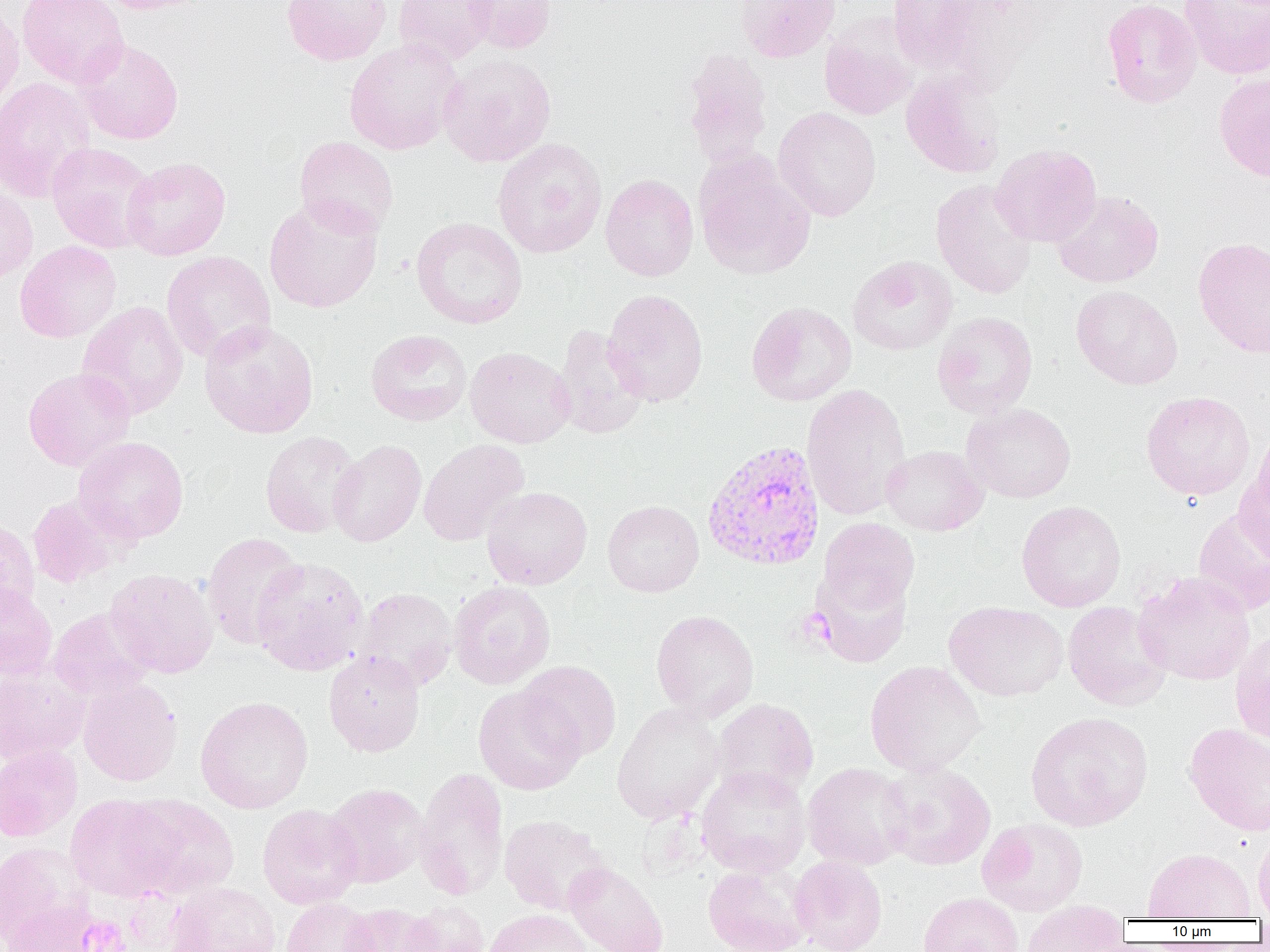

Summary:
  - Coordinate format: approximate bounding boxes as (x1,y1)-(x2,y2) corner pairs in pixels
  - Plasmodium vivax-infected red blood cell locations: (701,440)-(825,572)
  - Uninfected red blood cell locations: (17,0)-(129,88), (92,0)-(213,14), (281,0)-(391,65), (393,0)-(496,66), (463,0)-(556,54), (735,0)-(840,62), (888,0)-(977,71), (1102,0)-(1202,108), (1180,0)-(1270,79), (0,3)-(24,114), (820,24)-(917,120), (73,38)-(184,145), (343,38)-(464,155), (681,49)-(774,167), (438,53)-(557,167), (901,69)-(1006,178), (1215,73)-(1270,181), (0,77)-(97,203), (773,107)-(882,221), (294,136)-(399,237), (493,138)-(607,258), (46,142)-(157,253), (990,144)-(1102,247), (121,156)-(231,260), (695,158)-(816,280), (600,174)-(699,281), (930,180)-(1037,300), (0,182)-(38,284), (1051,190)-(1164,288), (263,196)-(384,314), (411,216)-(528,329), (1193,237)-(1270,358), (14,240)-(121,343), (161,251)-(276,363), (847,256)-(957,355), (1071,285)-(1183,389), (602,289)-(709,407), (76,301)-(188,419), (747,301)-(856,406), (932,311)-(1037,418), (199,319)-(319,439), (552,325)-(649,439), (365,329)-(472,426), (465,347)-(576,448), (23,367)-(136,471), (802,383)-(911,520), (1140,390)-(1256,501), (961,403)-(1076,503), (259,431)-(363,538), (73,436)-(189,544), (329,439)-(427,547), (418,439)-(529,546), (881,445)-(988,535), (1234,466)-(1270,566), (481,486)-(592,590), (27,495)-(124,588), (603,500)-(704,597), (1016,500)-(1126,611), (1192,507)-(1270,616), (0,516)-(40,619), (817,517)-(920,615), (201,532)-(306,649), (251,556)-(370,676), (810,566)-(913,667), (104,568)-(218,678), (1133,572)-(1255,685), (0,581)-(57,680), (449,581)-(555,689), (355,587)-(458,691), (943,601)-(1069,701), (1063,601)-(1171,710), (47,607)-(155,701), (650,610)-(759,720), (1230,629)-(1270,745), (323,650)-(425,757), (864,660)-(986,776), (517,661)-(622,760), (0,666)-(90,764), (77,676)-(183,786), (473,686)-(586,795), (195,695)-(314,814), (712,698)-(819,799), (611,702)-(725,824), (1025,711)-(1154,831), (1184,723)-(1270,836), (0,744)-(83,841), (227,748)-(342,870), (880,761)-(996,870), (802,762)-(913,870), (696,765)-(810,877), (415,767)-(509,899), (324,783)-(429,887), (65,794)-(181,901), (123,795)-(239,899), (257,804)-(363,909), (499,815)-(612,915), (977,818)-(1088,916), (1252,829)-(1270,919), (0,841)-(92,947), (1141,847)-(1256,920), (790,856)-(888,952), (564,862)-(668,952), (702,862)-(813,952), (165,881)-(281,952), (918,893)-(1024,952), (280,898)-(378,952), (0,899)-(105,952), (399,901)-(490,952), (339,903)-(442,952), (1019,903)-(1129,952), (483,908)-(595,952)
  - Platelet locations: (79,916)-(130,952)
  - Slide-level diagnosis: Plasmodium vivax
  - Magnification: 1000x
  - Preparation: thin blood film
  - Image size: 1270×952 pixels
  - Field of view: one of a larger specimen
  - Modality: light microscopy